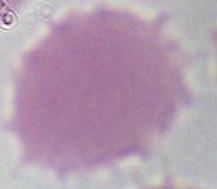

Micrograph. Captured at 1000x magnification. An erythrocyte is shown.